Point out each Plasmodium parasite.
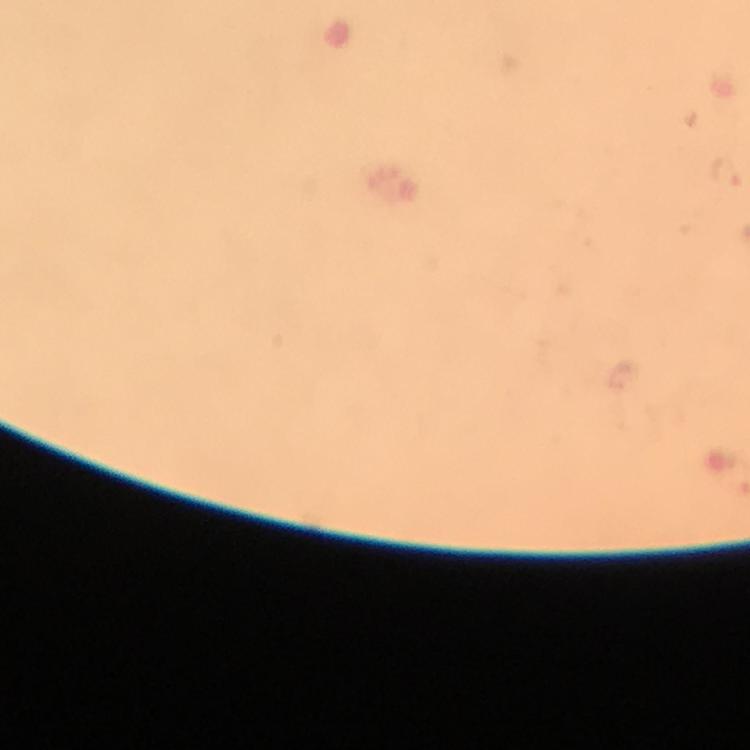

Approximate centers as {x, y} in pixels.
Plasmodium parasites: {726, 173}.

stain: Giemsa
context: from a malaria diagnostic workup
preparation: thick blood film
magnification: 100x
cropped_from: a single field of view
immersion_oil: applied
image_size: 750×750 pixels
capture: smartphone mounted on the microscope